Assess the morphology of the red blood cells.
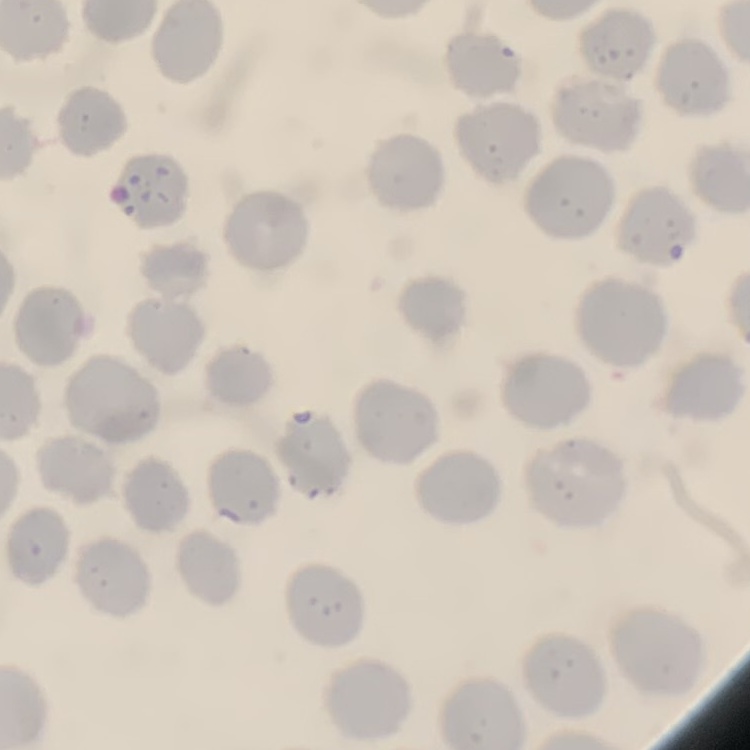
No rouleaux formation.

Summary:
  - Image type: one tile cut from a larger photomicrograph
  - Stain: Field's or Giemsa
  - Preparation: thin peripheral smear